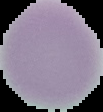

{
  "malaria_status": "uninfected",
  "image_size": "103×112 pixels",
  "preparation": "thin blood film",
  "image_type": "segmented cell region on a black background"
}